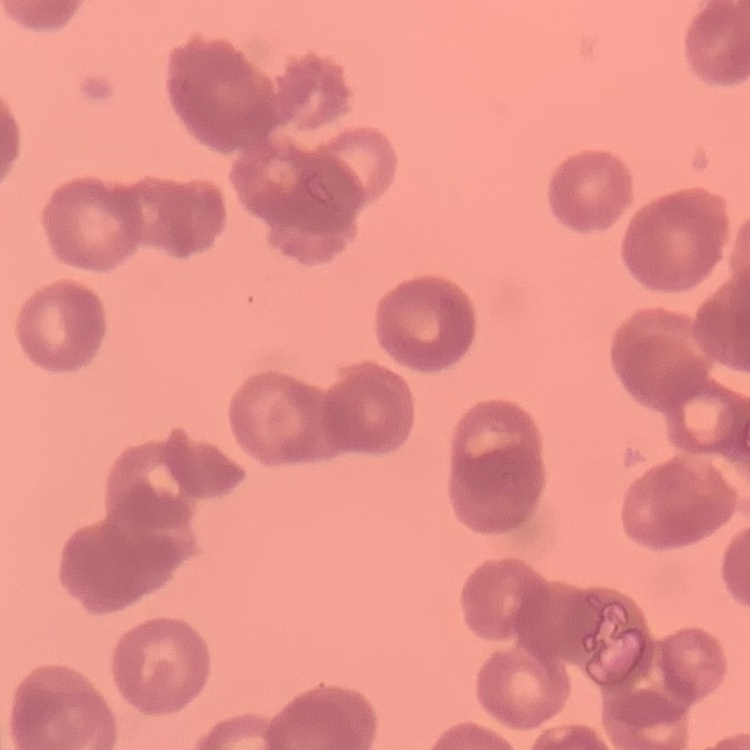
red blood cell morphology = rouleaux formation
preparation = thin blood film
image type = square crop of a larger photomicrograph
stain = Field's or Giemsa